Classify this cell by malaria status.
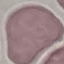

Uninfected.

stain = Giemsa
preparation = thin blood smear
image type = automatically extracted cell patch, resized to 64 × 64 pixels
capture = smartphone camera at the microscope eyepiece